Classify this cell by malaria status.
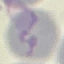
Uninfected.

Summary:
  - Image type: automatically extracted cell patch, resized to 64 × 64 pixels
  - Stain: Giemsa
  - Capture: smartphone camera at the microscope eyepiece
  - Preparation: thin blood film